State which parasite is depicted.
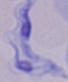

This is a trypanosome.

Captured at 1000x magnification. Micrograph.